Report the malaria status of this cell.
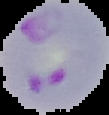

Parasitized.

image type = segmented cell region with the area outside set to black
image size = 109×115 pixels
preparation = thin blood smear